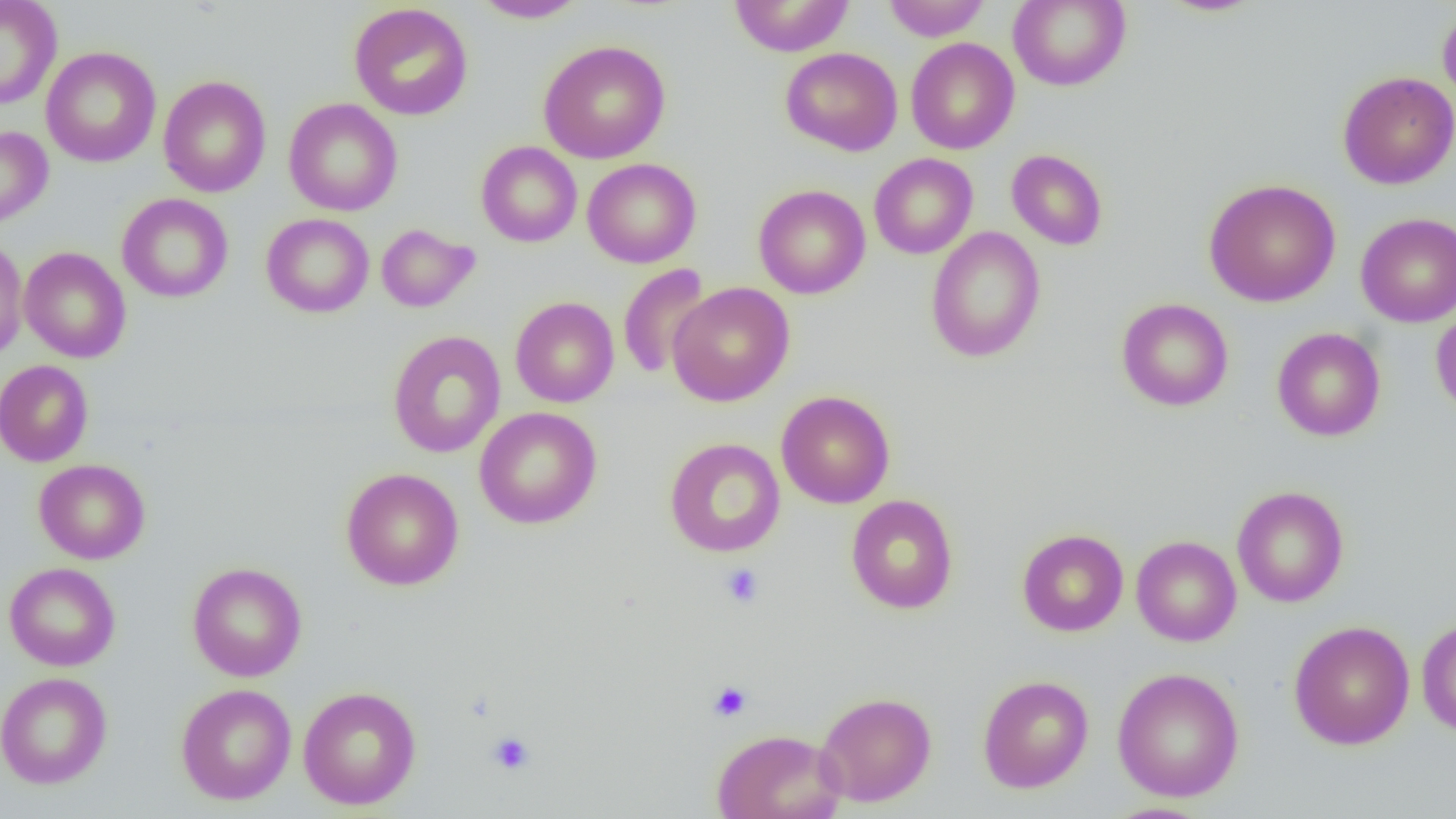

slide-level diagnosis = no evidence of blood parasites
uninfected red blood cell locations = approximate bounding boxes as named x1/y1/x2/y2 corners in pixels: (x1=0, y1=0, x2=62, y2=109), (x1=471, y1=0, x2=590, y2=23), (x1=728, y1=0, x2=855, y2=57), (x1=882, y1=0, x2=990, y2=41), (x1=1008, y1=0, x2=1131, y2=91), (x1=1154, y1=0, x2=1267, y2=17), (x1=349, y1=3, x2=473, y2=120), (x1=1437, y1=5, x2=1456, y2=109), (x1=905, y1=37, x2=1019, y2=154), (x1=538, y1=39, x2=671, y2=164), (x1=41, y1=46, x2=161, y2=168), (x1=780, y1=47, x2=903, y2=156), (x1=1337, y1=71, x2=1456, y2=189), (x1=158, y1=75, x2=271, y2=198), (x1=283, y1=98, x2=403, y2=216), (x1=0, y1=126, x2=53, y2=229), (x1=476, y1=141, x2=582, y2=247), (x1=1006, y1=149, x2=1108, y2=251), (x1=869, y1=153, x2=978, y2=259), (x1=582, y1=158, x2=701, y2=268), (x1=1204, y1=178, x2=1341, y2=307), (x1=754, y1=184, x2=870, y2=299), (x1=117, y1=193, x2=233, y2=303), (x1=1355, y1=212, x2=1456, y2=327), (x1=261, y1=213, x2=374, y2=317), (x1=376, y1=224, x2=480, y2=312), (x1=926, y1=227, x2=1046, y2=363), (x1=0, y1=235, x2=28, y2=363), (x1=19, y1=246, x2=131, y2=363), (x1=617, y1=263, x2=713, y2=381), (x1=667, y1=282, x2=795, y2=406), (x1=510, y1=297, x2=619, y2=407), (x1=1116, y1=298, x2=1234, y2=411), (x1=1431, y1=303, x2=1456, y2=420), (x1=1271, y1=327, x2=1386, y2=442), (x1=387, y1=330, x2=505, y2=458), (x1=0, y1=359, x2=93, y2=467), (x1=776, y1=390, x2=895, y2=508), (x1=474, y1=406, x2=602, y2=529), (x1=665, y1=438, x2=786, y2=557), (x1=34, y1=459, x2=150, y2=564), (x1=341, y1=467, x2=464, y2=591), (x1=1232, y1=486, x2=1349, y2=607), (x1=846, y1=494, x2=958, y2=614), (x1=1017, y1=529, x2=1129, y2=636), (x1=1131, y1=535, x2=1242, y2=646), (x1=187, y1=561, x2=307, y2=681), (x1=4, y1=562, x2=120, y2=671), (x1=1416, y1=618, x2=1456, y2=736), (x1=1288, y1=620, x2=1415, y2=750), (x1=1112, y1=667, x2=1245, y2=802), (x1=0, y1=671, x2=112, y2=789), (x1=978, y1=675, x2=1093, y2=792), (x1=176, y1=683, x2=296, y2=805), (x1=298, y1=687, x2=421, y2=809), (x1=815, y1=691, x2=937, y2=807), (x1=712, y1=728, x2=846, y2=819), (x1=1099, y1=802, x2=1215, y2=819)
modality = light microscopy
field of view = one of a larger specimen
platelet locations = approximate bounding boxes as named x1/y1/x2/y2 corners in pixels: (x1=721, y1=564, x2=764, y2=608), (x1=709, y1=682, x2=752, y2=721), (x1=486, y1=731, x2=535, y2=775)
image size = 1456×819 pixels
magnification = 1000x
preparation = thin blood smear